Classify this cell by malaria status.
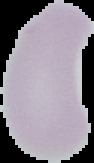

Uninfected.

Summary:
  - Image size: 94×163 pixels
  - Preparation: thin blood film
  - Image type: segmented cell region on a black background